Name the parasite shown.
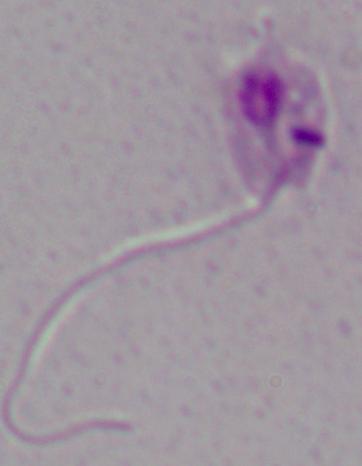

This is Leishmania.

modality: micrograph
magnification: 1000x